Locate every blood parasite and identify its species.
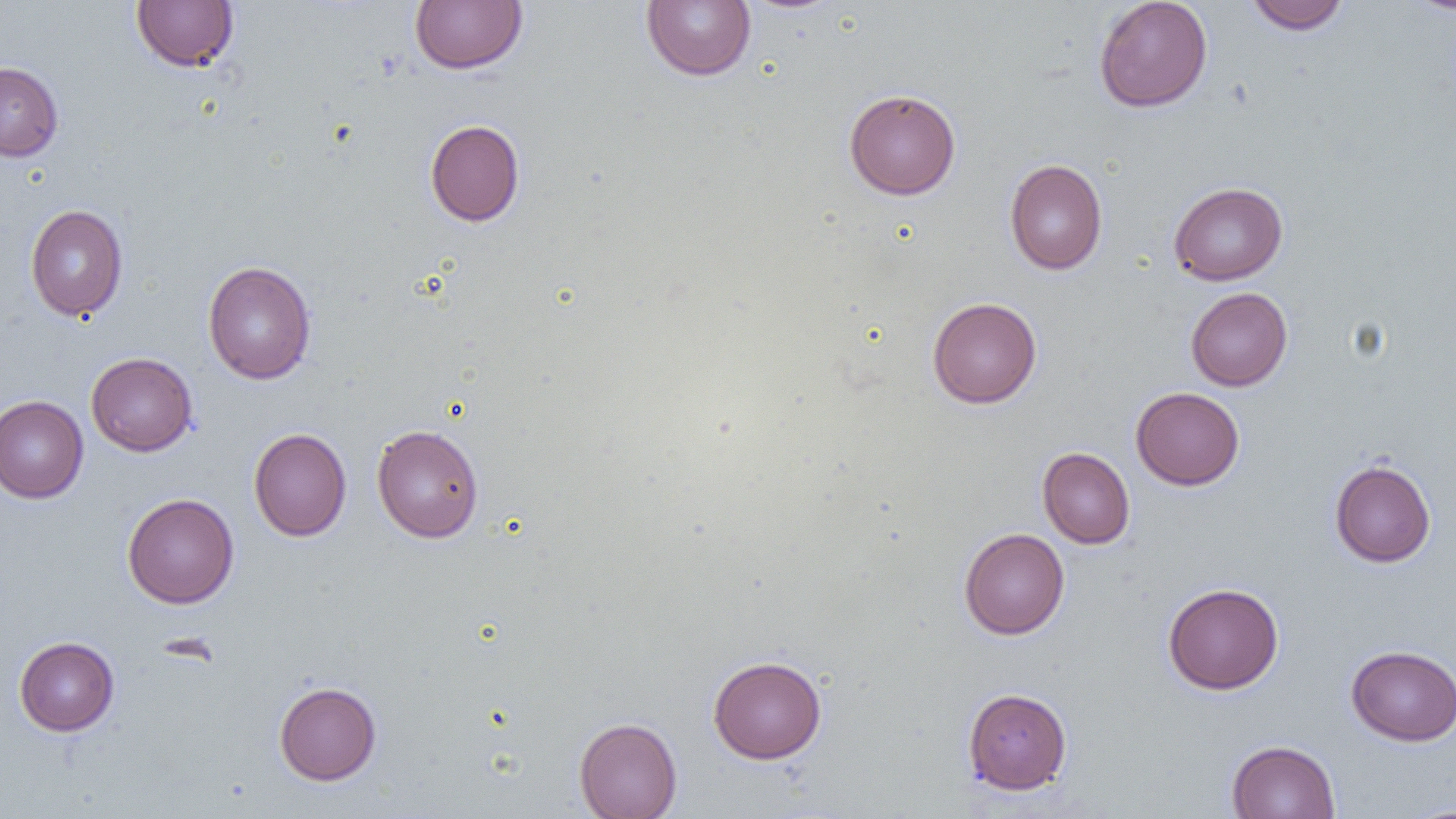
No blood parasites seen.

Summary:
  - Coordinate format: approximate bounding boxes as named x1/y1/x2/y2 corners in pixels
  - Uninfected red blood cell locations: (x1=131, y1=0, x2=240, y2=73), (x1=410, y1=0, x2=528, y2=74), (x1=641, y1=0, x2=756, y2=81), (x1=1094, y1=0, x2=1213, y2=112), (x1=1244, y1=0, x2=1350, y2=35), (x1=1404, y1=0, x2=1456, y2=16), (x1=0, y1=61, x2=63, y2=161), (x1=843, y1=88, x2=961, y2=200), (x1=425, y1=119, x2=525, y2=226), (x1=1005, y1=158, x2=1107, y2=275), (x1=1168, y1=181, x2=1288, y2=285), (x1=25, y1=204, x2=128, y2=321), (x1=203, y1=260, x2=316, y2=384), (x1=1185, y1=287, x2=1293, y2=391), (x1=927, y1=296, x2=1042, y2=408), (x1=86, y1=352, x2=198, y2=456), (x1=1131, y1=387, x2=1245, y2=490), (x1=0, y1=395, x2=88, y2=503), (x1=371, y1=424, x2=484, y2=543), (x1=249, y1=428, x2=352, y2=541), (x1=1037, y1=447, x2=1135, y2=549), (x1=1329, y1=459, x2=1436, y2=567), (x1=122, y1=492, x2=239, y2=608), (x1=958, y1=527, x2=1069, y2=639), (x1=1162, y1=582, x2=1284, y2=694), (x1=14, y1=636, x2=119, y2=736), (x1=1346, y1=644, x2=1456, y2=746), (x1=708, y1=655, x2=827, y2=764), (x1=274, y1=681, x2=382, y2=785), (x1=962, y1=687, x2=1072, y2=794), (x1=574, y1=716, x2=683, y2=819), (x1=1225, y1=739, x2=1340, y2=819), (x1=1403, y1=803, x2=1456, y2=818)
  - Slide-level diagnosis: negative for blood parasites
  - Magnification: 1000x
  - Field of view: single
  - Preparation: thin blood smear
  - Modality: light microscopy
  - Image size: 1456×819 pixels